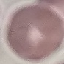

{
  "result": "no malaria parasites seen",
  "stain": "Giemsa",
  "preparation": "thin smear",
  "image_type": "cell patch, automatically extracted from a larger field of view and resized to 64 × 64 pixels",
  "capture": "smartphone through the microscope eyepiece"
}